Evaluate for Plasmodium parasites.
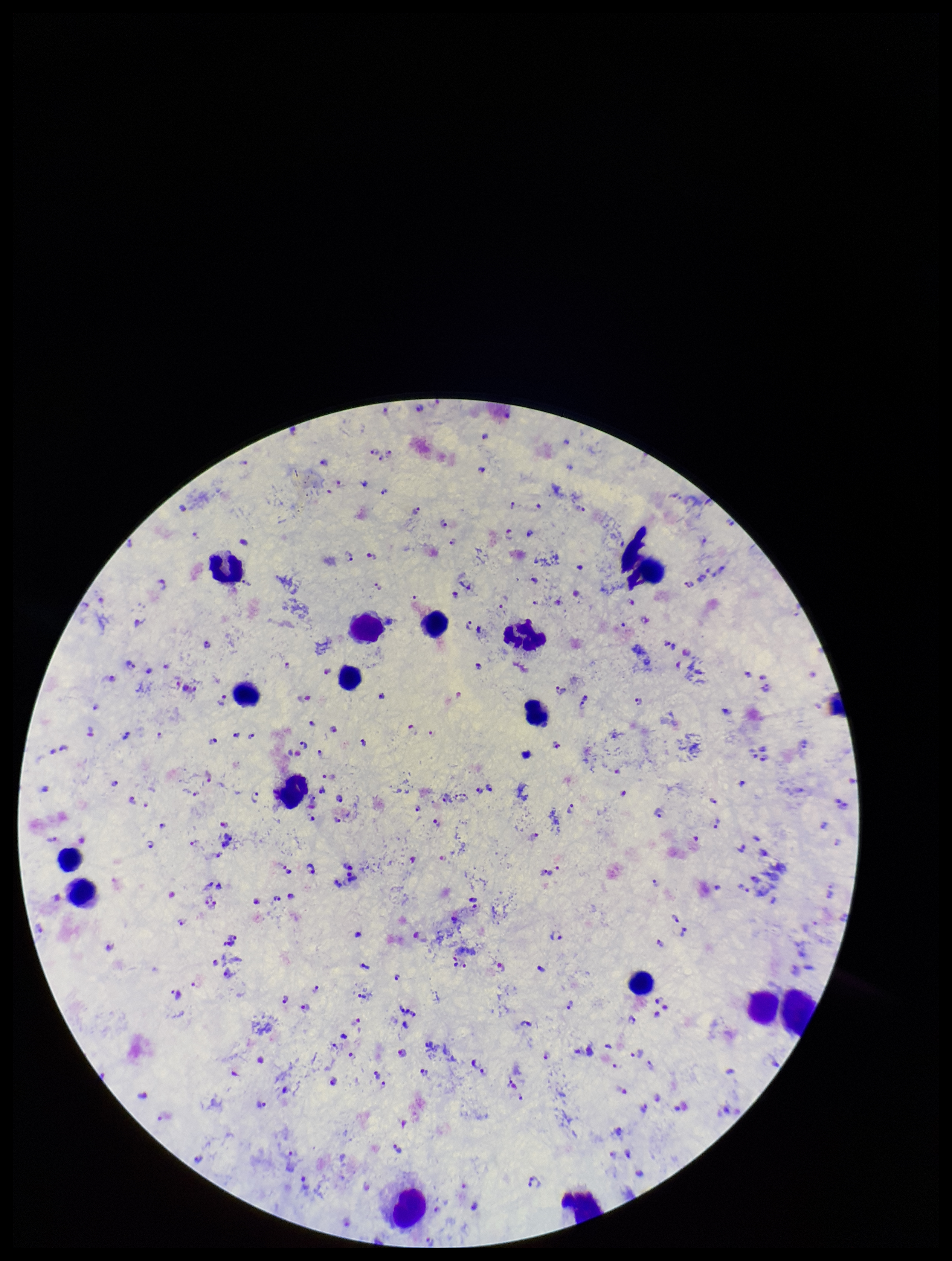
Seen.

Summary:
  - Capture: smartphone photograph through the microscope eyepiece
  - Leukocyte count: 16
  - Species reported for this patient: Plasmodium falciparum
  - Patient malaria status: infected
  - Preparation: thick
  - Field of view: one from this slide
  - Image size: 952×1261 pixels
  - Stain: Giemsa
  - Parasite count: 200